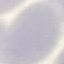

Summary:
  - Result: no malaria parasites seen
  - Capture: smartphone through the microscope eyepiece
  - Stain: Giemsa
  - Preparation: thin blood smear
  - Image type: cell patch, automatically extracted from a larger field of view and resized to 64 × 64 pixels